Assess this cell for malaria.
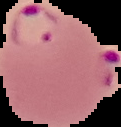
Parasitized.

Summary:
  - Image type: cell region segmented out of the field of view; surrounding area masked to black
  - Preparation: thin blood film
  - Image size: 121×127 pixels